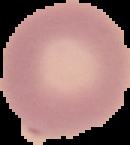
Image is 130×145 pixels. Segmented cell region on a black background. Result: no malaria parasites detected. From a thin blood smear.